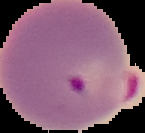 From a thin blood smear. Image is 145×133 pixels. Cell region segmented out of the field of view; the surrounding area is masked to black. Malaria status: parasitized.